Assess this cell for malaria.
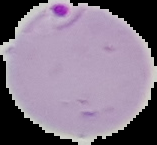
Parasitized.

Image is 157×145 pixels. Segmented cell region on a black background. From a thin blood smear.